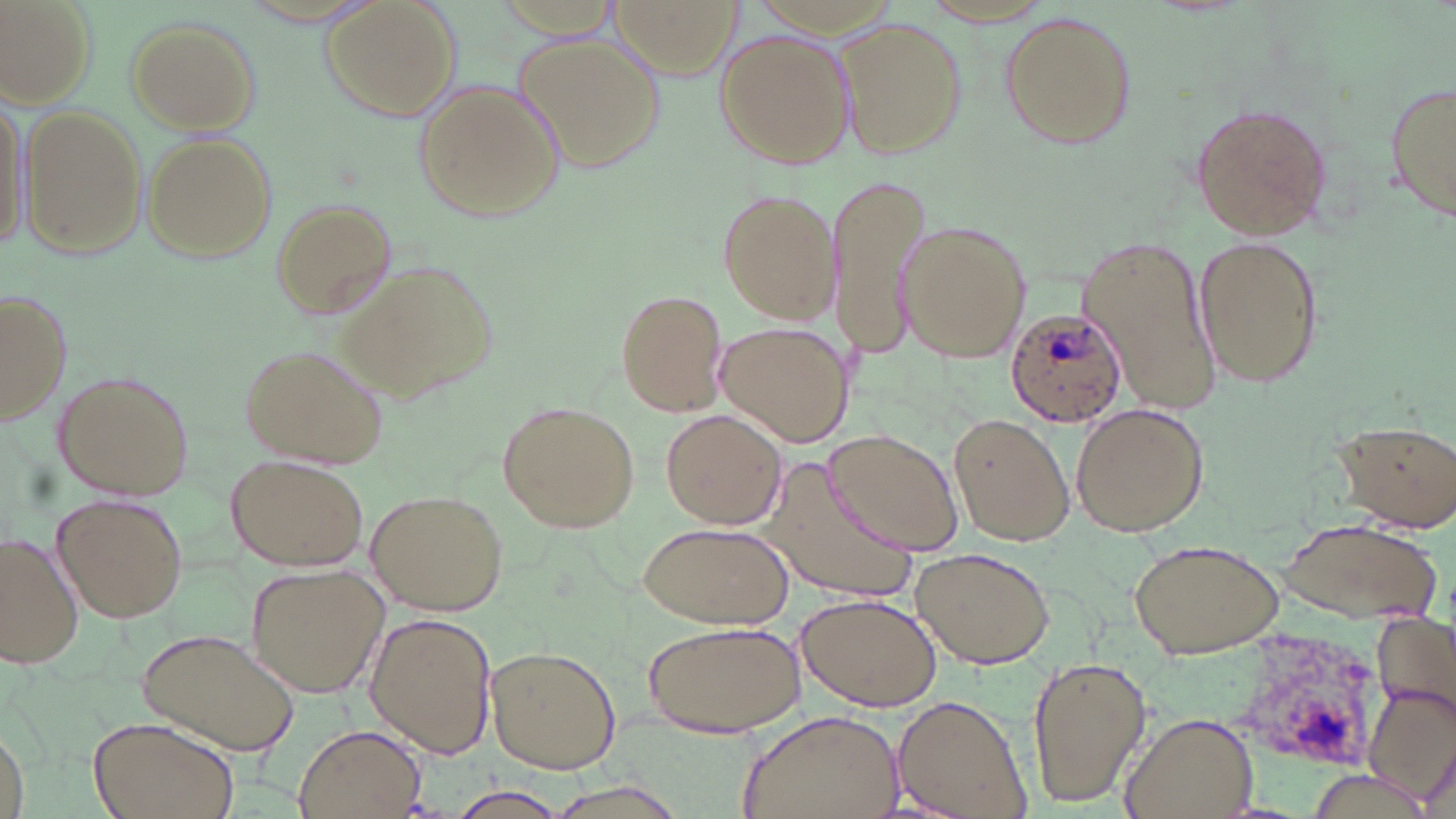

Approximate bounding boxes as (x1, y1, x2, y2) in pixels. Plasmodium ovale-infected red blood cell locations: (1002, 307, 1126, 425). Uninfected red blood cell locations: (3, 0, 96, 105), (321, 0, 460, 120), (609, 0, 740, 78), (999, 13, 1135, 148), (835, 16, 966, 161), (124, 18, 260, 133), (715, 28, 853, 171), (515, 33, 668, 176), (414, 78, 561, 223), (1385, 81, 1456, 219), (2, 91, 32, 255), (19, 104, 148, 261), (1189, 105, 1332, 242), (142, 132, 276, 264), (825, 172, 935, 356), (720, 186, 840, 326), (270, 198, 398, 317), (899, 221, 1029, 362), (1192, 231, 1326, 392), (1079, 233, 1217, 410), (341, 256, 497, 399), (615, 287, 727, 417), (1, 289, 69, 427), (716, 321, 855, 449), (242, 344, 387, 468), (54, 369, 194, 500), (499, 401, 640, 534), (1069, 403, 1207, 535), (660, 409, 784, 530), (949, 414, 1074, 545), (1331, 419, 1456, 531), (825, 431, 962, 556), (229, 453, 371, 571), (765, 461, 921, 602), (366, 490, 510, 615), (52, 492, 187, 622), (1283, 519, 1440, 622), (639, 521, 793, 631), (1, 533, 83, 669), (1127, 537, 1286, 659), (912, 546, 1054, 670), (247, 562, 388, 697), (796, 590, 942, 712), (367, 613, 496, 759), (1373, 615, 1456, 727), (642, 618, 806, 738), (139, 628, 299, 755), (485, 646, 620, 774), (1026, 654, 1150, 806), (1363, 683, 1456, 807), (894, 695, 1032, 819), (737, 707, 905, 819), (1120, 710, 1260, 819), (87, 715, 240, 819), (1, 724, 28, 819), (295, 725, 425, 817), (440, 789, 575, 819). Slide-level diagnosis: Plasmodium ovale. One field of a larger specimen. Thin blood smear. Image is 1456×819 pixels. 1000x magnification. Light microscopy. May-Grünwald-Giemsa stain.